Report the malaria status of this cell.
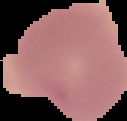

It is uninfected.

The area outside the segmented cell region is set to black. Image is 127×121 pixels. From a thin blood smear.